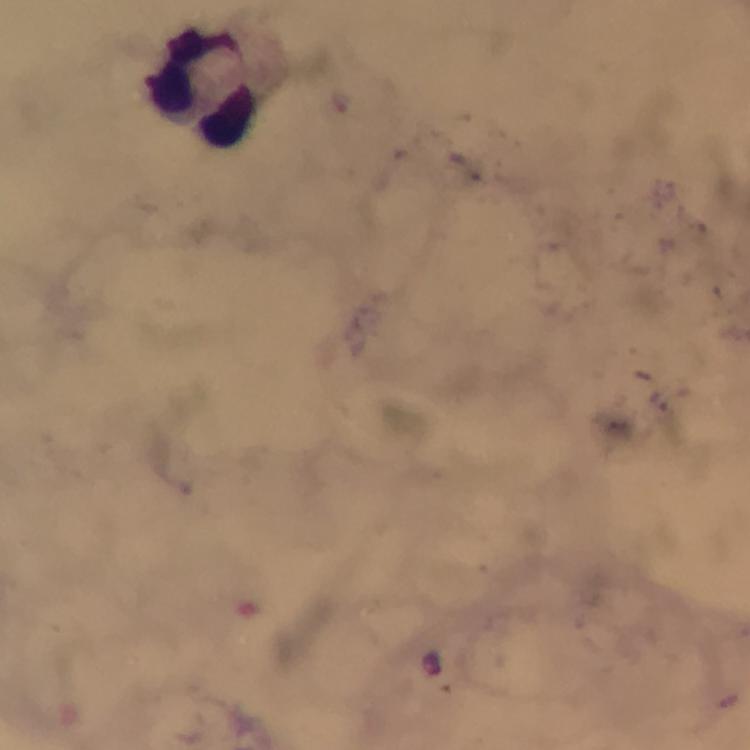

capture = smartphone mounted on the microscope
cropped from = one field of view
Plasmodium parasites = none detected
context = from a malaria diagnostic workup
preparation = thick blood film
immersion oil = used
leukocyte locations = approximate centers as [x, y] in pixels: [208, 90]
image size = 750×750 pixels
stain = Giemsa
magnification = 100x